Give a bounding box for every malaria parasite.
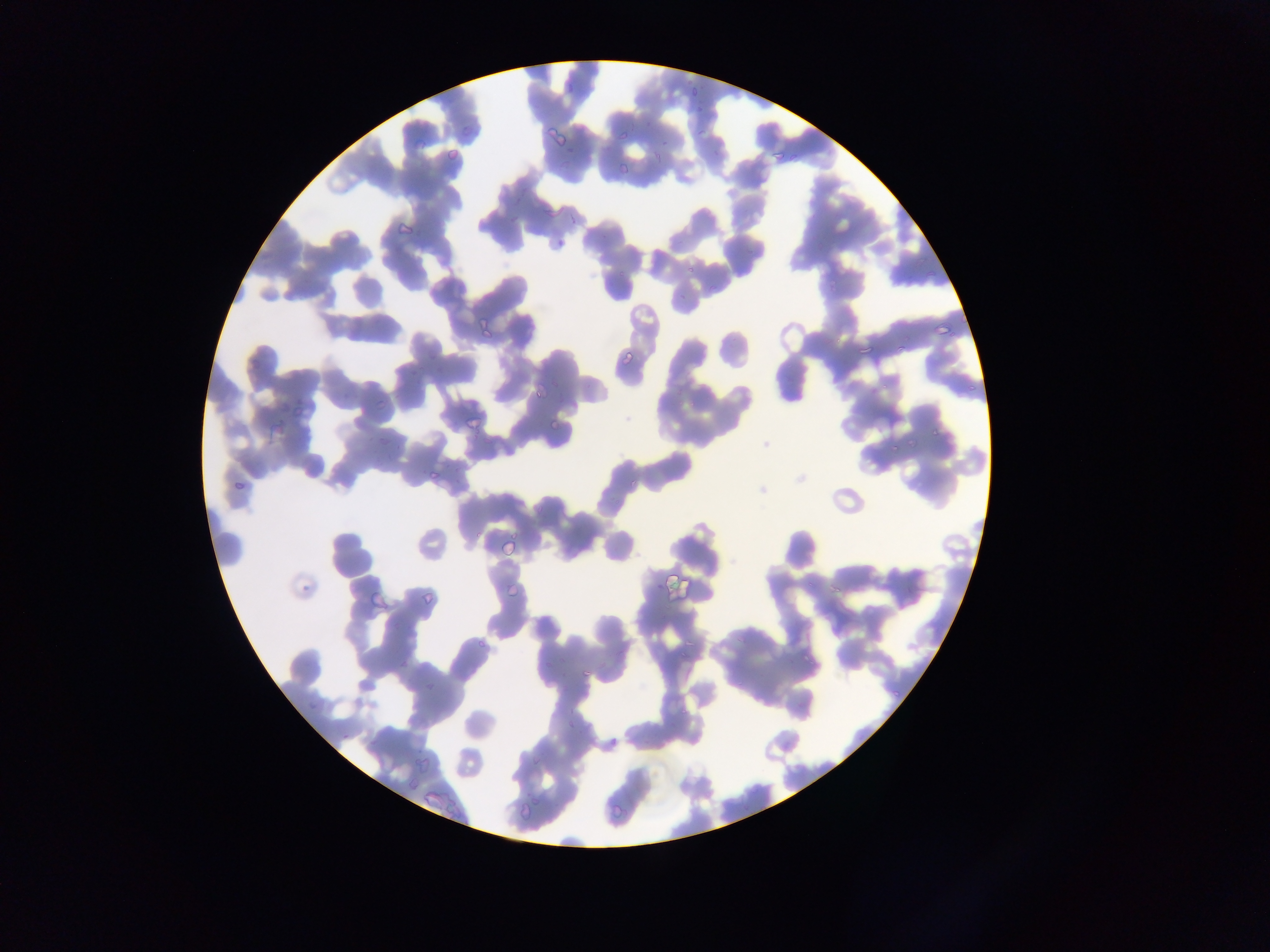
Approximate bounding boxes as {left, top, right, bottom} in pixels.
Malaria parasites: {690, 86, 701, 97}, {456, 117, 483, 142}, {548, 126, 569, 146}, {616, 130, 630, 142}, {769, 148, 783, 165}, {444, 149, 460, 163}, {618, 163, 629, 175}, {537, 197, 562, 215}, {397, 223, 412, 236}, {477, 319, 493, 335}, {934, 319, 952, 337}, {621, 348, 634, 361}, {529, 380, 553, 400}, {371, 397, 383, 410}, {459, 414, 484, 431}, {545, 420, 560, 433}, {270, 421, 286, 437}, {903, 437, 919, 450}, {423, 466, 442, 482}, {231, 477, 246, 493}, {499, 534, 519, 555}, {663, 570, 688, 592}, {506, 579, 525, 600}, {416, 589, 433, 608}, {577, 664, 592, 678}, {565, 720, 576, 731}, {417, 753, 430, 773}, {520, 796, 538, 814}, {606, 805, 625, 822}.

Summary:
  - Field of view: single
  - Capture: mobile-phone photograph through a microscope
  - Preparation: thin blood film
  - Country: Ghana
  - Image size: 1270×952 pixels